Outline each blood parasite and name the species.
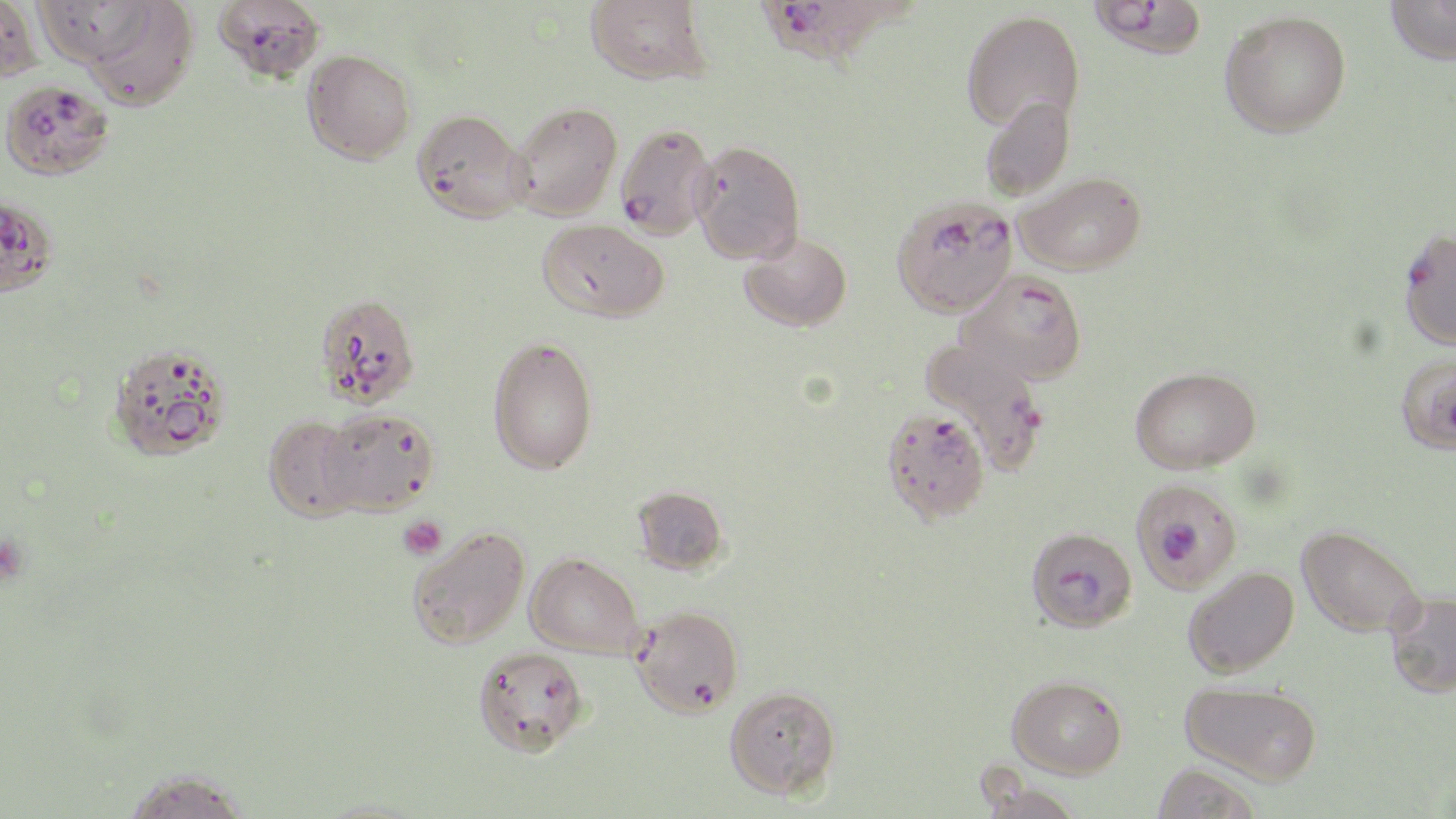

Approximate bounding boxes as [x1, y1, x2, y2] in pixels.
Plasmodium falciparum-infected red blood cells: [213, 0, 325, 82], [1088, 0, 1208, 59], [757, 2, 887, 70], [0, 79, 115, 181], [614, 123, 716, 239], [0, 194, 59, 298], [891, 195, 1018, 319], [1398, 228, 1456, 351], [958, 270, 1088, 385], [919, 336, 1049, 470], [881, 407, 990, 523], [1129, 477, 1242, 593], [1026, 526, 1137, 633], [631, 604, 744, 717].
No Plasmodium ovale, Plasmodium malariae, Plasmodium vivax, Babesia divergens, or Trypanosoma brucei observed.

Platelet locations: [398, 514, 447, 559]. Uninfected red blood cell locations: [0, 0, 43, 83], [586, 0, 711, 85], [1385, 0, 1456, 65], [32, 2, 160, 66], [80, 2, 200, 111], [961, 9, 1084, 131], [1220, 10, 1351, 138], [303, 49, 416, 164], [980, 96, 1075, 201], [507, 101, 622, 221], [412, 109, 529, 223], [689, 140, 806, 264], [1014, 171, 1147, 275], [538, 219, 669, 322], [740, 232, 852, 331], [314, 291, 421, 408], [488, 335, 598, 475], [105, 342, 232, 462], [1395, 353, 1456, 455], [1128, 365, 1261, 473], [318, 407, 439, 515], [263, 414, 368, 522], [632, 485, 729, 576], [407, 525, 530, 649], [1297, 525, 1425, 637], [525, 552, 644, 658], [1183, 566, 1299, 677], [1385, 591, 1456, 697], [473, 646, 590, 757], [1007, 674, 1127, 778], [1180, 680, 1322, 784], [724, 685, 841, 799], [1151, 763, 1264, 819], [117, 767, 254, 819]. Slide-level diagnosis: Plasmodium falciparum. Image is 1456×819 pixels. Captured at 1000x magnification. Optical microscopy. Thin blood smear. Single field of view. May-Grünwald-Giemsa-stained preparation.